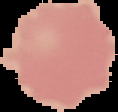
result = no Plasmodium parasites seen
image size = 118×112 pixels
image type = segmented cell region with the area outside set to black
preparation = thin blood smear